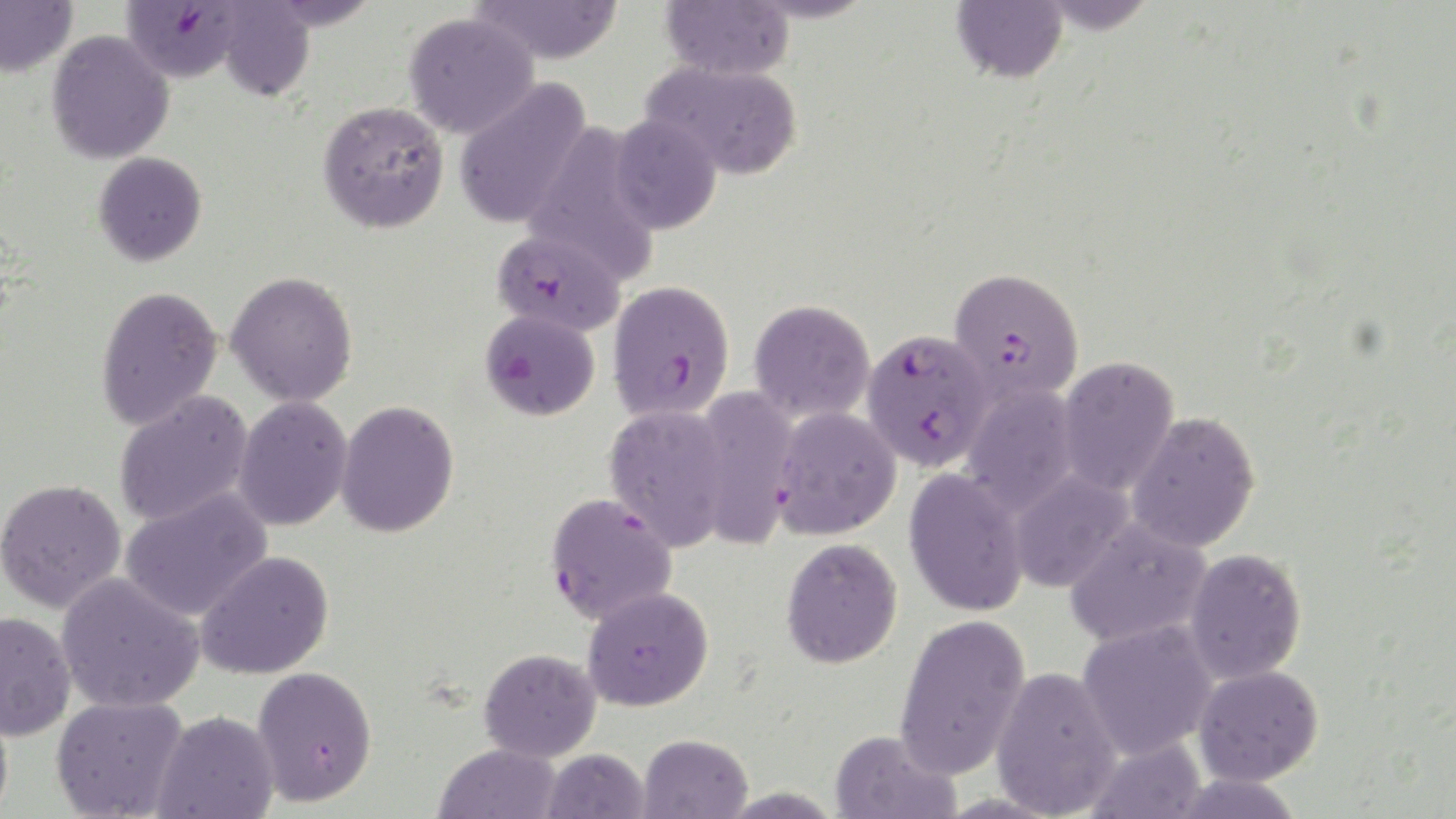
slide_level_diagnosis: Plasmodium falciparum
preparation: thin blood film
uninfected_red_blood_cell_locations: 'approximate bounding boxes as (x1,y1)-(x2,y2) corner pairs in pixels: (0,0)-(78,77), (469,0)-(624,65), (660,0)-(794,81), (951,0)-(1068,83), (1033,0)-(1161,34), (214,2)-(315,101), (404,12)-(539,140), (46,30)-(175,164), (642,60)-(803,181), (453,78)-(593,229), (318,100)-(449,233), (608,114)-(722,234), (522,124)-(661,283), (93,152)-(207,266), (226,270)-(359,408), (95,285)-(224,430), (749,299)-(875,423), (1056,355)-(1179,496), (961,385)-(1081,516), (692,387)-(801,549), (114,391)-(253,527), (232,395)-(353,531), (336,400)-(460,538), (603,403)-(733,551), (772,406)-(901,539), (1125,410)-(1262,552), (903,468)-(1030,617), (1007,469)-(1134,592), (0,478)-(126,613), (120,487)-(273,622), (1065,517)-(1212,648), (780,537)-(903,668), (1183,547)-(1307,683), (196,550)-(335,679), (56,572)-(205,713), (583,585)-(714,711), (0,612)-(76,741), (893,613)-(1032,777), (1077,620)-(1218,759), (478,648)-(601,762), (991,665)-(1123,818), (1194,665)-(1323,785), (251,666)-(377,806), (51,695)-(188,819), (151,710)-(279,819), (829,729)-(960,819), (638,733)-(752,819), (1083,736)-(1207,819), (433,743)-(561,819), (542,748)-(649,819)'
plasmodium_falciparum_infected_red_blood_cell_locations: 'approximate bounding boxes as (x1,y1)-(x2,y2) corner pairs in pixels: (121,1)-(246,83), (491,228)-(625,335), (947,266)-(1083,406), (608,280)-(735,421), (479,309)-(600,420), (861,328)-(995,471), (546,492)-(678,626)'
magnification: 1000x
stain: May-Grünwald-Giemsa
image_size: 1456×819 pixels
field_of_view: one of a larger specimen
modality: optical microscopy